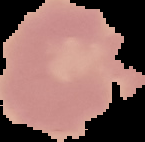
{
  "malaria_status": "uninfected",
  "image_type": "segmented cell region with the area outside set to black",
  "preparation": "thin blood smear",
  "image_size": "145×142 pixels"
}